Name the parasite shown.
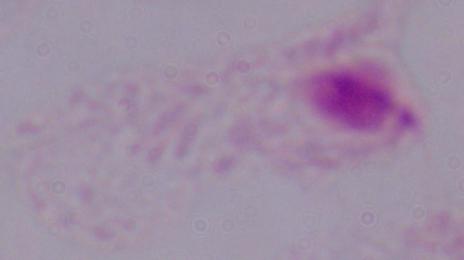
This is a trichomonad.

modality = micrograph
magnification = 1000x